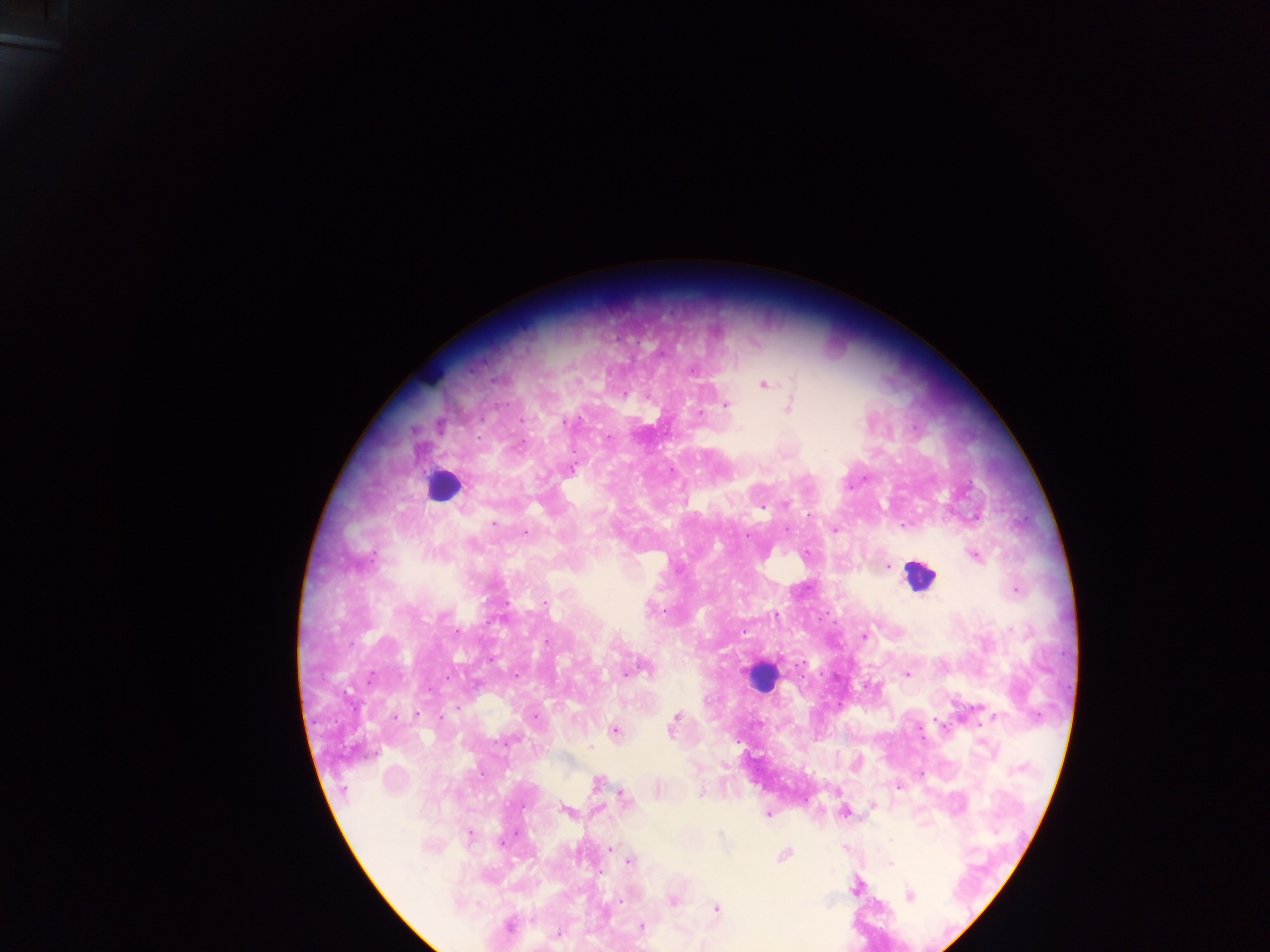

{
  "plasmodium_parasite_locations": "approximate centers as x y in pixels: 493 379; 764 385; 624 394; 726 405; 789 406; 701 414; 523 420; 565 421; 740 429; 608 437; 521 444; 571 469; 785 504; 810 516; 494 523; 836 529; 525 532; 975 556; 373 557; 888 566; 1016 591; 545 604; 457 630; 744 632; 863 636; 547 642; 639 670; 628 672; 907 674; 371 677; 416 714; 676 716; 536 717; 396 718; 937 722; 672 728; 615 732; 590 747; 597 782; 899 786; 701 793; 624 799; 872 804; 566 811; 768 814; 721 834; 469 835; 892 839; 611 849; 784 855; 629 862; 890 864; 855 887; 909 896; 673 900; 621 901; 717 908; 509 925; 641 926; 557 935",
  "capture": "mobile-phone photograph through a microscope",
  "field_of_view": "single",
  "preparation": "thick blood film",
  "country": "Ghana",
  "leukocyte_locations": "approximate centers as x y in pixels: 430 378; 442 485; 919 575; 762 677",
  "image_size": "1270×952 pixels"
}